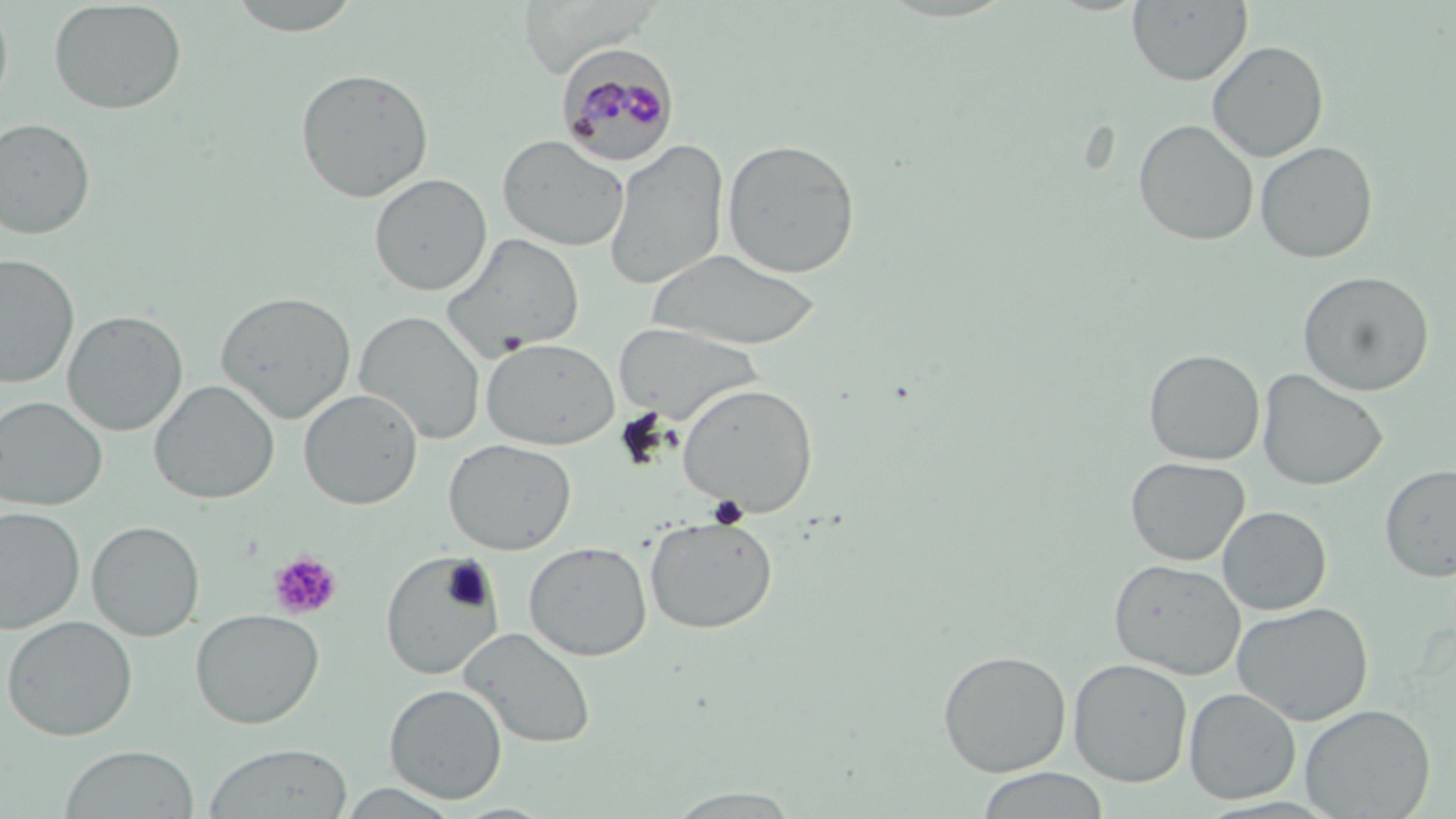
Summary:
  - Coordinate format: approximate bounding boxes as (x1,y1)-(x2,y2) corner pairs in pixels
  - Plasmodium malariae-infected red blood cell locations: (556,45)-(680,167)
  - Uninfected red blood cell locations: (0,0)-(14,114), (223,0)-(366,36), (48,1)-(187,114), (1127,1)-(1252,86), (1207,41)-(1329,162), (295,67)-(434,203), (0,117)-(96,239), (1133,119)-(1258,246), (498,135)-(630,252), (722,137)-(860,278), (604,139)-(729,290), (1255,141)-(1378,264), (369,172)-(492,296), (441,233)-(585,361), (648,248)-(823,350), (0,254)-(79,389), (1297,270)-(1435,396), (215,291)-(356,424), (62,310)-(187,435), (354,311)-(486,444), (614,322)-(761,423), (481,337)-(621,449), (1143,348)-(1265,465), (1257,368)-(1388,491), (149,379)-(279,505), (676,383)-(819,517), (298,388)-(423,510), (0,395)-(107,510), (443,437)-(577,555), (1125,456)-(1250,565), (1380,464)-(1456,582), (0,506)-(86,633), (1217,506)-(1332,615), (644,516)-(778,634), (86,520)-(205,641), (524,541)-(653,661), (379,551)-(506,681), (1109,558)-(1246,679), (1233,602)-(1374,725), (190,608)-(325,728), (1,615)-(138,740), (459,626)-(597,749), (937,649)-(1072,777), (1068,658)-(1193,786), (384,683)-(507,803), (1184,687)-(1301,804), (1299,704)-(1436,818), (201,742)-(354,819), (58,745)-(200,818), (975,768)-(1112,819), (334,783)-(463,818), (665,788)-(803,818)
  - Platelet locations: (707,495)-(750,529), (268,550)-(342,620)
  - Slide-level diagnosis: Plasmodium malariae
  - Stain: May-Grünwald-Giemsa
  - Preparation: thin blood film
  - Image size: 1456×819 pixels
  - Magnification: 1000x
  - Field of view: one of a larger specimen
  - Modality: optical microscopy